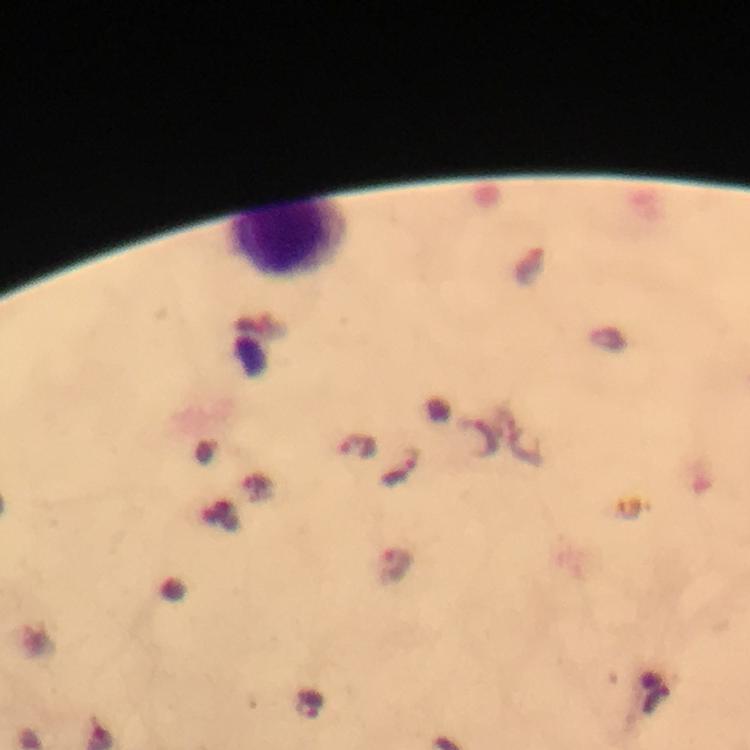
Approximate centers as {x, y} in pixels.
Summary:
  - Malaria parasite locations: {480, 437}, {402, 467}, {395, 565}, {308, 704}
  - Leukocyte locations: {286, 242}
  - Immersion oil: used
  - Capture: smartphone mounted on the microscope
  - Stain: Giemsa
  - Context: from a diagnostic examination for malaria
  - Cropped from: one field of view
  - Image size: 750×750 pixels
  - Preparation: thick smear
  - Magnification: 100x